State which parasite is depicted.
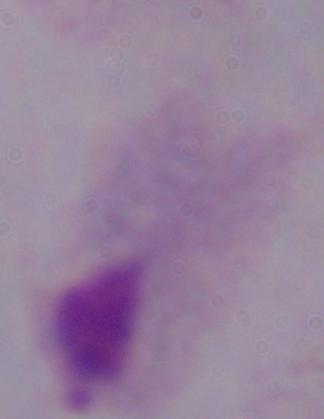
A trichomonad.

Summary:
  - Modality: micrograph
  - Magnification: 1000x